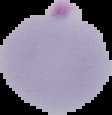
Image is 112×115 pixels. Segmented cell region on a black background. Result: Plasmodium parasites detected. From a thin blood smear.